Locate the P. falciparum-infected red blood cells and any of indeterminate infection status.
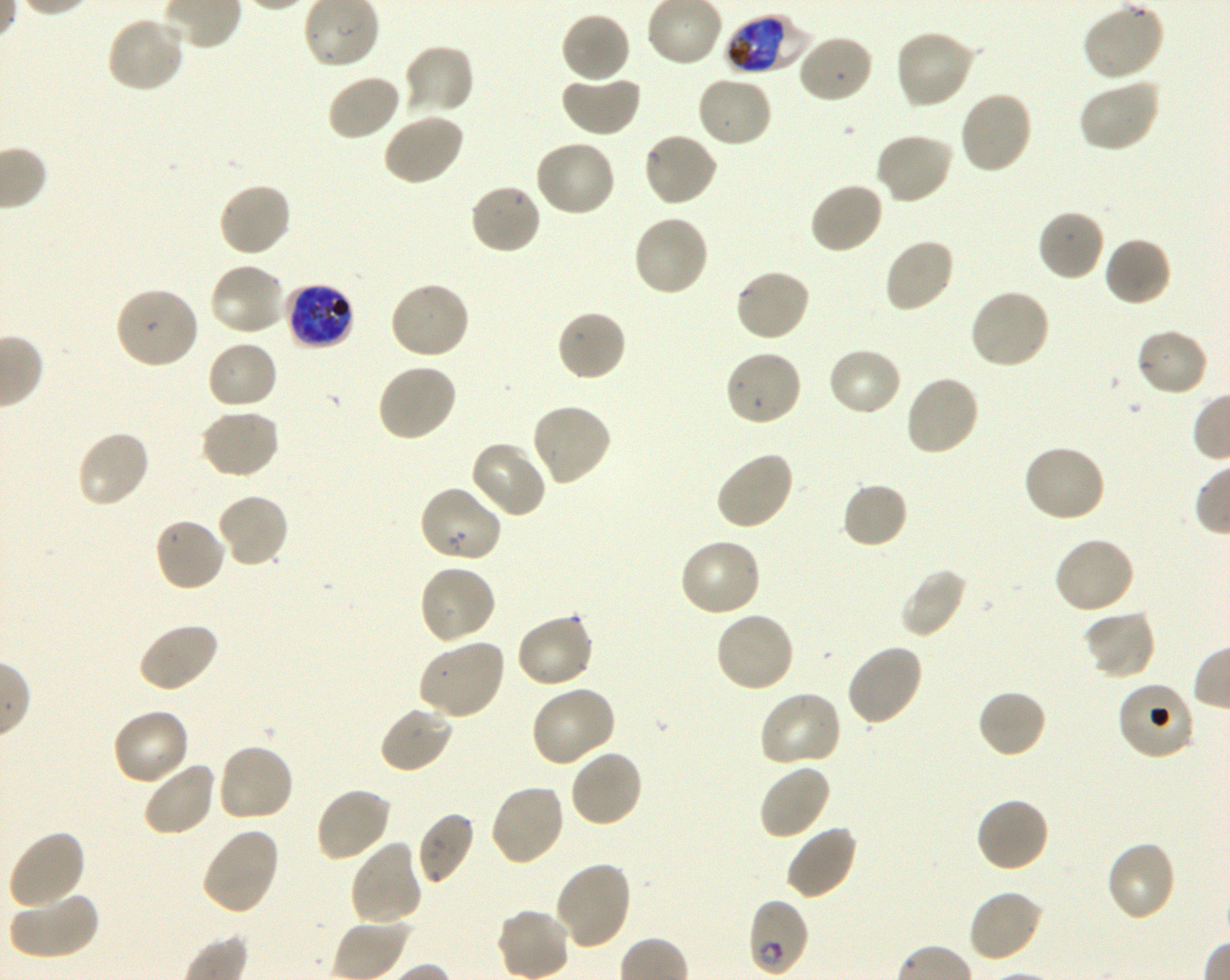
Approximate bounding rectangles given as corner coordinates in pixels from the top-left. Not every red blood cell is marked. A life-cycle stage — or a range of stages, where the recorded stages span more than one — follows each staged infected red blood cell.
Infected red blood cells: (x1=725, y1=13, x2=810, y2=76) early trophozoite to late schizont; (x1=285, y1=283, x2=355, y2=350) late trophozoite to late schizont; (x1=747, y1=898, x2=809, y2=977) early ring to early trophozoite.
Red blood cells of indeterminate infection status: (x1=1117, y1=680, x2=1196, y2=761).

Summary:
  - Locations of uninfected red blood cells: (x1=1082, y1=1, x2=1164, y2=82), (x1=560, y1=11, x2=631, y2=84), (x1=106, y1=14, x2=187, y2=94), (x1=894, y1=29, x2=977, y2=111), (x1=796, y1=33, x2=874, y2=105), (x1=402, y1=43, x2=475, y2=118), (x1=326, y1=74, x2=402, y2=142), (x1=561, y1=74, x2=642, y2=138), (x1=696, y1=75, x2=773, y2=149), (x1=1077, y1=78, x2=1162, y2=153), (x1=957, y1=89, x2=1034, y2=175), (x1=382, y1=113, x2=464, y2=187), (x1=641, y1=131, x2=719, y2=207), (x1=874, y1=132, x2=955, y2=205), (x1=533, y1=139, x2=616, y2=219), (x1=809, y1=181, x2=885, y2=256), (x1=217, y1=182, x2=293, y2=259), (x1=468, y1=183, x2=543, y2=256), (x1=1036, y1=208, x2=1106, y2=282), (x1=632, y1=214, x2=709, y2=298), (x1=1103, y1=236, x2=1173, y2=308), (x1=882, y1=237, x2=956, y2=314), (x1=208, y1=262, x2=287, y2=338), (x1=734, y1=268, x2=811, y2=343), (x1=388, y1=279, x2=471, y2=359), (x1=114, y1=286, x2=201, y2=370), (x1=969, y1=287, x2=1051, y2=370), (x1=556, y1=309, x2=628, y2=383), (x1=1135, y1=327, x2=1209, y2=397), (x1=206, y1=340, x2=278, y2=411), (x1=826, y1=346, x2=903, y2=418), (x1=723, y1=347, x2=804, y2=427), (x1=375, y1=363, x2=457, y2=442), (x1=904, y1=375, x2=981, y2=457), (x1=530, y1=403, x2=613, y2=486), (x1=198, y1=408, x2=281, y2=480), (x1=76, y1=430, x2=152, y2=510), (x1=469, y1=441, x2=547, y2=519), (x1=1021, y1=444, x2=1106, y2=524), (x1=715, y1=450, x2=795, y2=532), (x1=841, y1=481, x2=909, y2=549), (x1=417, y1=484, x2=504, y2=564), (x1=215, y1=492, x2=290, y2=570), (x1=153, y1=516, x2=228, y2=593), (x1=1052, y1=535, x2=1135, y2=615), (x1=678, y1=537, x2=763, y2=618), (x1=418, y1=562, x2=497, y2=645), (x1=899, y1=566, x2=966, y2=638), (x1=1083, y1=609, x2=1157, y2=680), (x1=714, y1=610, x2=796, y2=693), (x1=514, y1=612, x2=594, y2=690), (x1=137, y1=622, x2=221, y2=693), (x1=418, y1=638, x2=507, y2=720), (x1=845, y1=643, x2=924, y2=728), (x1=529, y1=684, x2=617, y2=768), (x1=976, y1=688, x2=1048, y2=760), (x1=757, y1=690, x2=842, y2=769), (x1=379, y1=704, x2=454, y2=774), (x1=112, y1=708, x2=191, y2=787), (x1=216, y1=742, x2=295, y2=823), (x1=568, y1=748, x2=644, y2=828), (x1=142, y1=760, x2=219, y2=838), (x1=757, y1=763, x2=831, y2=841), (x1=488, y1=783, x2=565, y2=868), (x1=314, y1=786, x2=392, y2=863), (x1=975, y1=796, x2=1050, y2=873), (x1=416, y1=811, x2=475, y2=886), (x1=784, y1=824, x2=858, y2=901), (x1=199, y1=827, x2=280, y2=916), (x1=7, y1=828, x2=85, y2=909), (x1=349, y1=840, x2=424, y2=927), (x1=1105, y1=840, x2=1177, y2=923), (x1=553, y1=861, x2=632, y2=950), (x1=967, y1=888, x2=1044, y2=964), (x1=8, y1=891, x2=98, y2=961)
  - Donor blood group: O+
  - Objective: 100x, oil immersion, numerical aperture 1.30
  - Stain: Giemsa
  - Preparation: thin blood smear
  - Culture: P. falciparum strain 3D7, shaking, in vitro
  - Image size: 1230×980 pixels
  - Field of view: single